Give the extent of all Plasmodium falciparum-infected red blood cells.
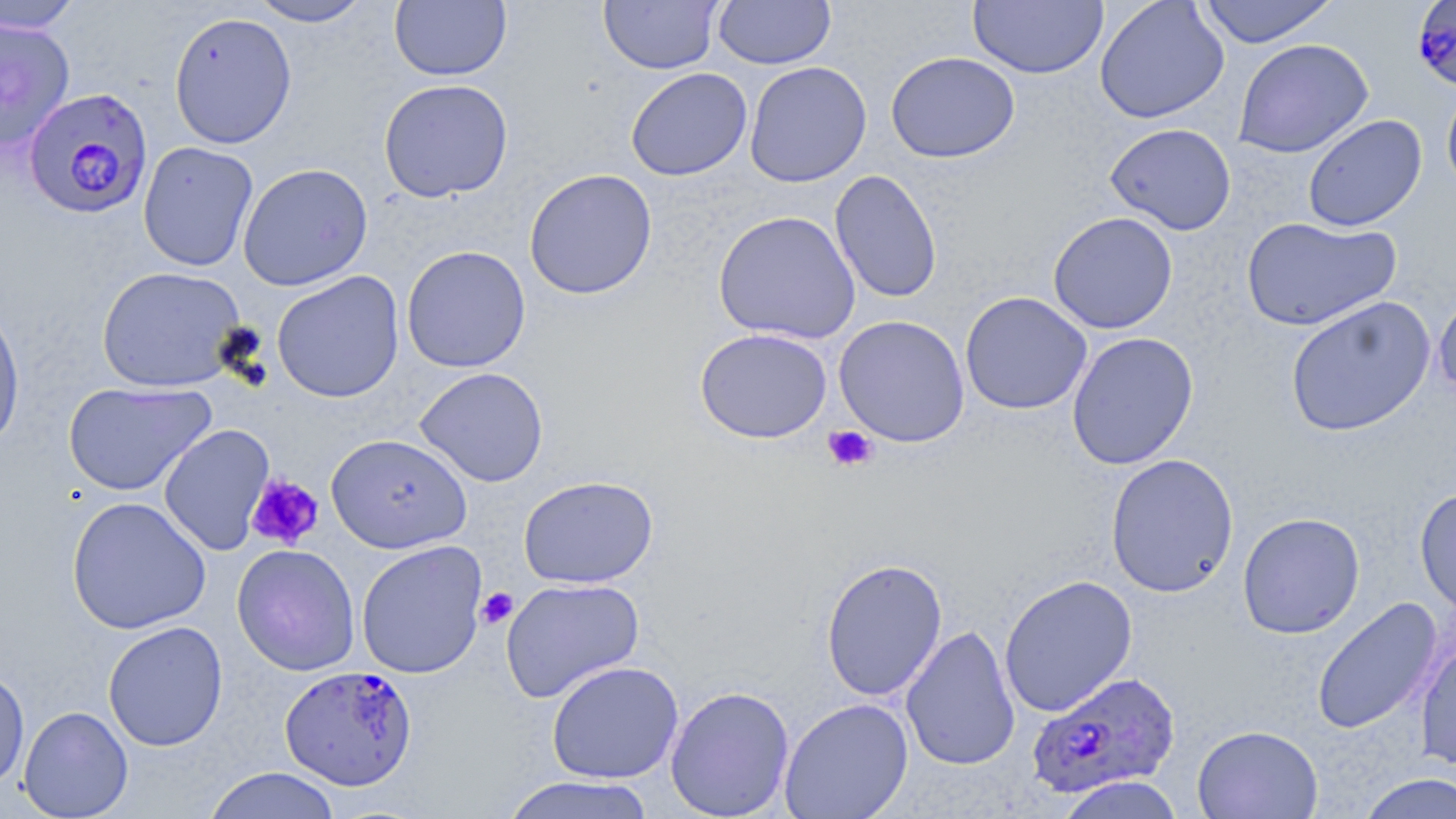
Approximate bounding boxes as named x1/y1/x2/y2 corners in pixels.
Plasmodium falciparum-infected red blood cells: (x1=1412, y1=3, x2=1456, y2=96), (x1=26, y1=87, x2=156, y2=219), (x1=276, y1=666, x2=414, y2=791), (x1=1023, y1=669, x2=1178, y2=798).

Summary:
  - Platelet locations: (x1=823, y1=425, x2=878, y2=473), (x1=246, y1=474, x2=324, y2=549), (x1=475, y1=587, x2=518, y2=630)
  - Uninfected red blood cell locations: (x1=248, y1=0, x2=372, y2=27), (x1=598, y1=0, x2=722, y2=74), (x1=713, y1=0, x2=835, y2=69), (x1=1094, y1=0, x2=1229, y2=124), (x1=1196, y1=0, x2=1340, y2=47), (x1=0, y1=1, x2=84, y2=34), (x1=390, y1=1, x2=512, y2=82), (x1=968, y1=1, x2=1108, y2=79), (x1=168, y1=11, x2=297, y2=149), (x1=0, y1=18, x2=75, y2=151), (x1=1233, y1=38, x2=1373, y2=159), (x1=886, y1=51, x2=1020, y2=163), (x1=744, y1=61, x2=872, y2=187), (x1=626, y1=67, x2=752, y2=181), (x1=378, y1=78, x2=514, y2=202), (x1=1441, y1=80, x2=1456, y2=199), (x1=1302, y1=114, x2=1427, y2=232), (x1=1105, y1=122, x2=1236, y2=235), (x1=137, y1=141, x2=259, y2=272), (x1=237, y1=162, x2=374, y2=290), (x1=524, y1=168, x2=658, y2=299), (x1=829, y1=169, x2=942, y2=303), (x1=713, y1=210, x2=861, y2=344), (x1=1048, y1=211, x2=1178, y2=334), (x1=1241, y1=216, x2=1401, y2=332), (x1=401, y1=246, x2=531, y2=373), (x1=95, y1=265, x2=248, y2=393), (x1=272, y1=270, x2=405, y2=403), (x1=1433, y1=290, x2=1456, y2=405), (x1=960, y1=292, x2=1092, y2=415), (x1=1285, y1=296, x2=1436, y2=437), (x1=0, y1=299, x2=26, y2=455), (x1=833, y1=315, x2=970, y2=447), (x1=694, y1=327, x2=832, y2=444), (x1=1066, y1=331, x2=1199, y2=471), (x1=414, y1=367, x2=548, y2=487), (x1=63, y1=380, x2=215, y2=496), (x1=158, y1=424, x2=275, y2=555), (x1=326, y1=433, x2=472, y2=553), (x1=1105, y1=452, x2=1240, y2=598), (x1=518, y1=475, x2=658, y2=589), (x1=1415, y1=487, x2=1456, y2=619), (x1=67, y1=496, x2=212, y2=635), (x1=1237, y1=511, x2=1365, y2=639), (x1=356, y1=540, x2=488, y2=679), (x1=232, y1=544, x2=360, y2=676), (x1=820, y1=557, x2=948, y2=701), (x1=999, y1=574, x2=1139, y2=717), (x1=499, y1=577, x2=645, y2=703), (x1=1311, y1=597, x2=1442, y2=735), (x1=103, y1=621, x2=228, y2=751), (x1=900, y1=624, x2=1020, y2=771), (x1=1415, y1=637, x2=1456, y2=771), (x1=546, y1=660, x2=684, y2=783), (x1=0, y1=667, x2=30, y2=791), (x1=665, y1=685, x2=795, y2=818), (x1=779, y1=697, x2=913, y2=818), (x1=18, y1=705, x2=133, y2=818), (x1=1192, y1=725, x2=1323, y2=819), (x1=203, y1=767, x2=342, y2=819), (x1=1357, y1=772, x2=1456, y2=819), (x1=500, y1=775, x2=658, y2=819), (x1=1056, y1=775, x2=1185, y2=819)
  - Slide-level diagnosis: Plasmodium falciparum
  - Modality: light microscopy
  - Preparation: thin blood film
  - Magnification: 1000x
  - Stain: May-Grünwald-Giemsa
  - Field of view: single
  - Image size: 1456×819 pixels